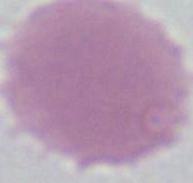
Summary:
  - Modality: photomicrograph
  - Identification: red blood cell
  - Magnification: 1000x